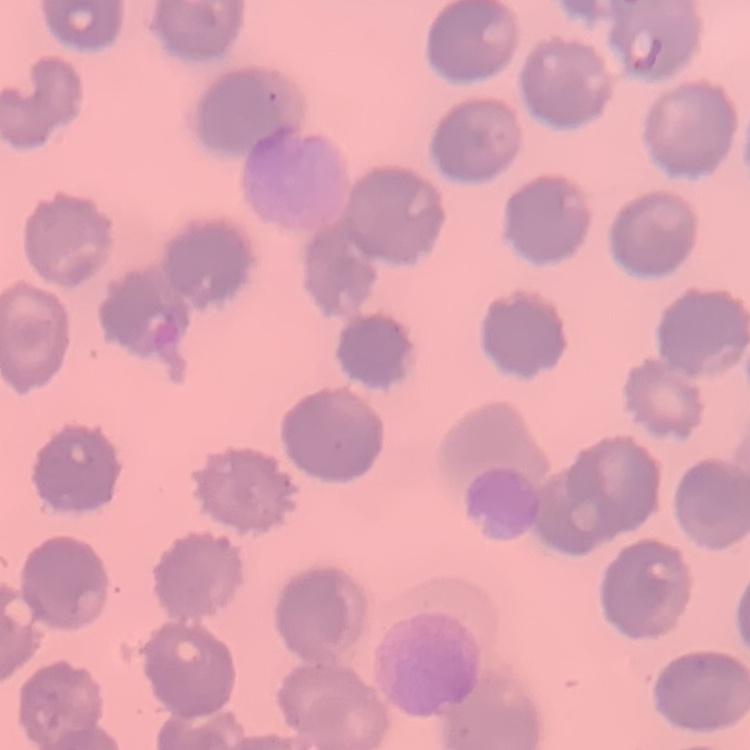

red_blood_cell_morphology: no rouleaux formation
image_type: one tile cut from a larger photomicrograph
stain: Field's or Giemsa
preparation: thin peripheral smear